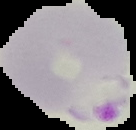
Summary:
  - Malaria status: parasitized
  - Image size: 136×130 pixels
  - Preparation: thin blood smear
  - Image type: segmented cell region on a black background